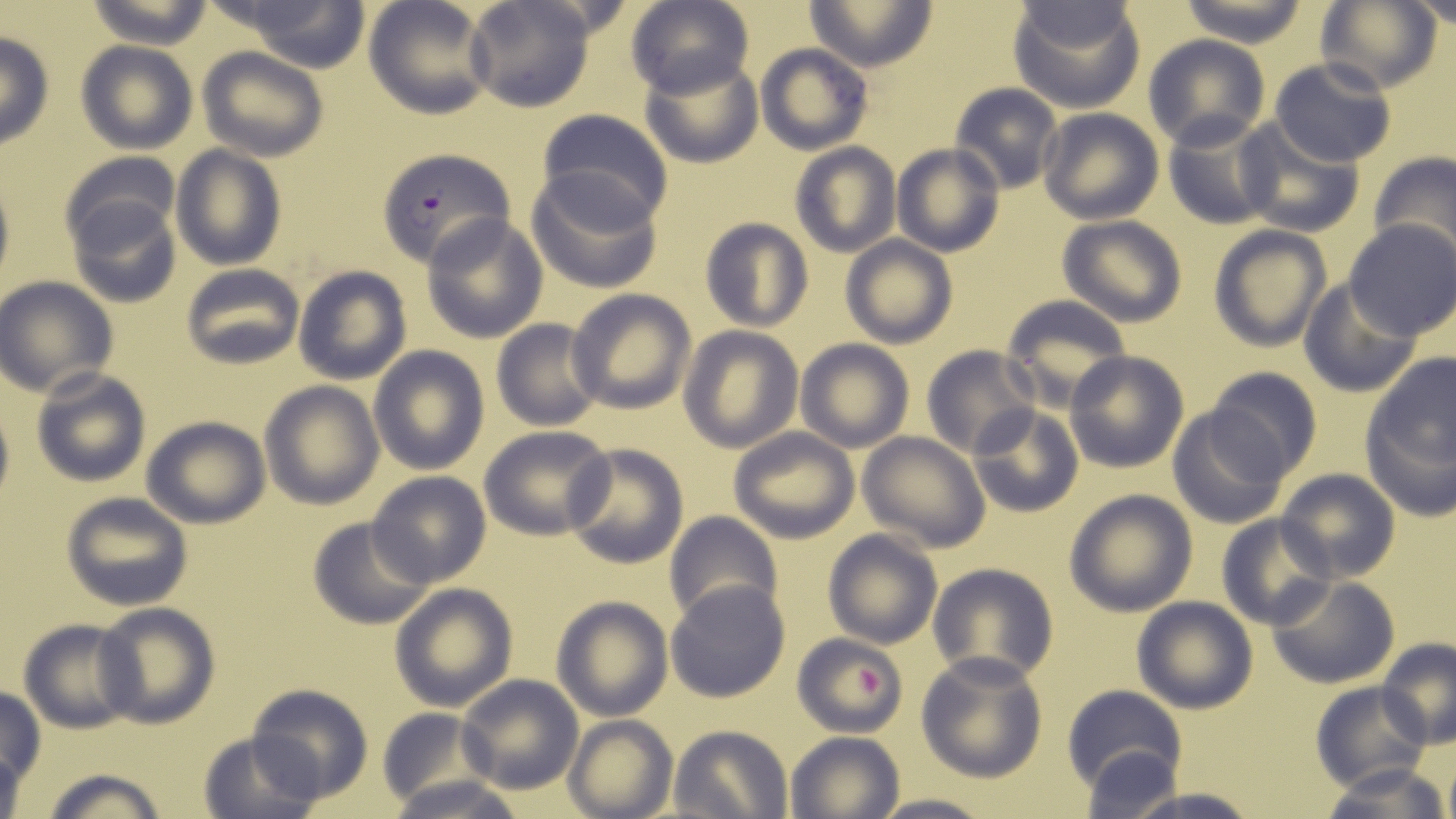

Approximate bounding boxes as [x1, y1, x2, y2] in pixels. Plasmodium falciparum-infected red blood cell locations: [373, 147, 515, 268]. Platelet locations: [853, 666, 887, 700]. Uninfected red blood cell locations: [238, 0, 372, 71], [464, 0, 596, 112], [625, 0, 753, 98], [804, 0, 937, 70], [1008, 0, 1146, 111], [1177, 0, 1313, 47], [1402, 0, 1456, 30], [82, 1, 216, 48], [363, 1, 495, 120], [1314, 1, 1442, 95], [0, 33, 54, 149], [1143, 36, 1270, 151], [74, 40, 197, 153], [755, 42, 872, 154], [197, 48, 329, 162], [638, 55, 762, 168], [1270, 57, 1396, 168], [949, 83, 1063, 193], [536, 108, 672, 224], [1037, 109, 1163, 224], [1162, 115, 1280, 231], [1235, 119, 1365, 238], [789, 143, 899, 257], [892, 144, 1005, 257], [169, 145, 286, 269], [1367, 153, 1456, 265], [58, 154, 181, 259], [524, 168, 664, 294], [64, 191, 183, 309], [421, 213, 549, 342], [1056, 215, 1188, 327], [699, 218, 813, 332], [1345, 220, 1456, 341], [1208, 225, 1331, 352], [841, 236, 956, 348], [180, 265, 303, 370], [292, 266, 411, 384], [0, 276, 117, 397], [1298, 278, 1422, 397], [567, 288, 696, 414], [1000, 296, 1130, 411], [490, 318, 604, 431], [677, 325, 802, 451], [795, 340, 915, 453], [921, 345, 1039, 457], [368, 346, 489, 474], [1063, 350, 1190, 474], [1360, 353, 1454, 503], [1206, 365, 1321, 478], [31, 368, 152, 488], [258, 380, 385, 510], [0, 396, 14, 518], [968, 404, 1083, 516], [1167, 406, 1291, 529], [141, 416, 269, 528], [480, 428, 612, 539], [729, 428, 860, 544], [859, 431, 987, 550], [563, 442, 689, 570], [99, 445, 234, 586], [1276, 469, 1399, 582], [367, 472, 491, 587], [1063, 489, 1198, 616], [62, 491, 194, 610], [663, 510, 782, 622], [1215, 514, 1336, 629], [308, 515, 434, 629], [822, 529, 942, 648], [926, 561, 1060, 686], [1266, 575, 1399, 689], [666, 581, 790, 703], [390, 583, 517, 711], [1131, 596, 1258, 713], [551, 597, 673, 720], [94, 602, 221, 729], [18, 619, 141, 733], [792, 632, 907, 738], [1377, 637, 1456, 749], [916, 652, 1047, 782], [455, 674, 584, 793], [1309, 682, 1430, 791], [244, 683, 372, 804], [1061, 685, 1188, 797], [0, 687, 46, 798], [375, 708, 494, 807], [562, 715, 678, 819], [668, 725, 794, 819], [197, 729, 324, 818], [786, 730, 907, 819], [1078, 744, 1189, 818], [1442, 754, 1456, 819], [1320, 764, 1449, 819], [41, 767, 170, 819], [383, 774, 530, 819], [1117, 788, 1265, 819], [870, 793, 992, 819]. Slide-level diagnosis: Plasmodium falciparum. One field of a larger specimen. Captured at 1000x magnification. Image is 1456×819 pixels. May-Grünwald-Giemsa-stained preparation. Thin blood smear. Optical microscopy.